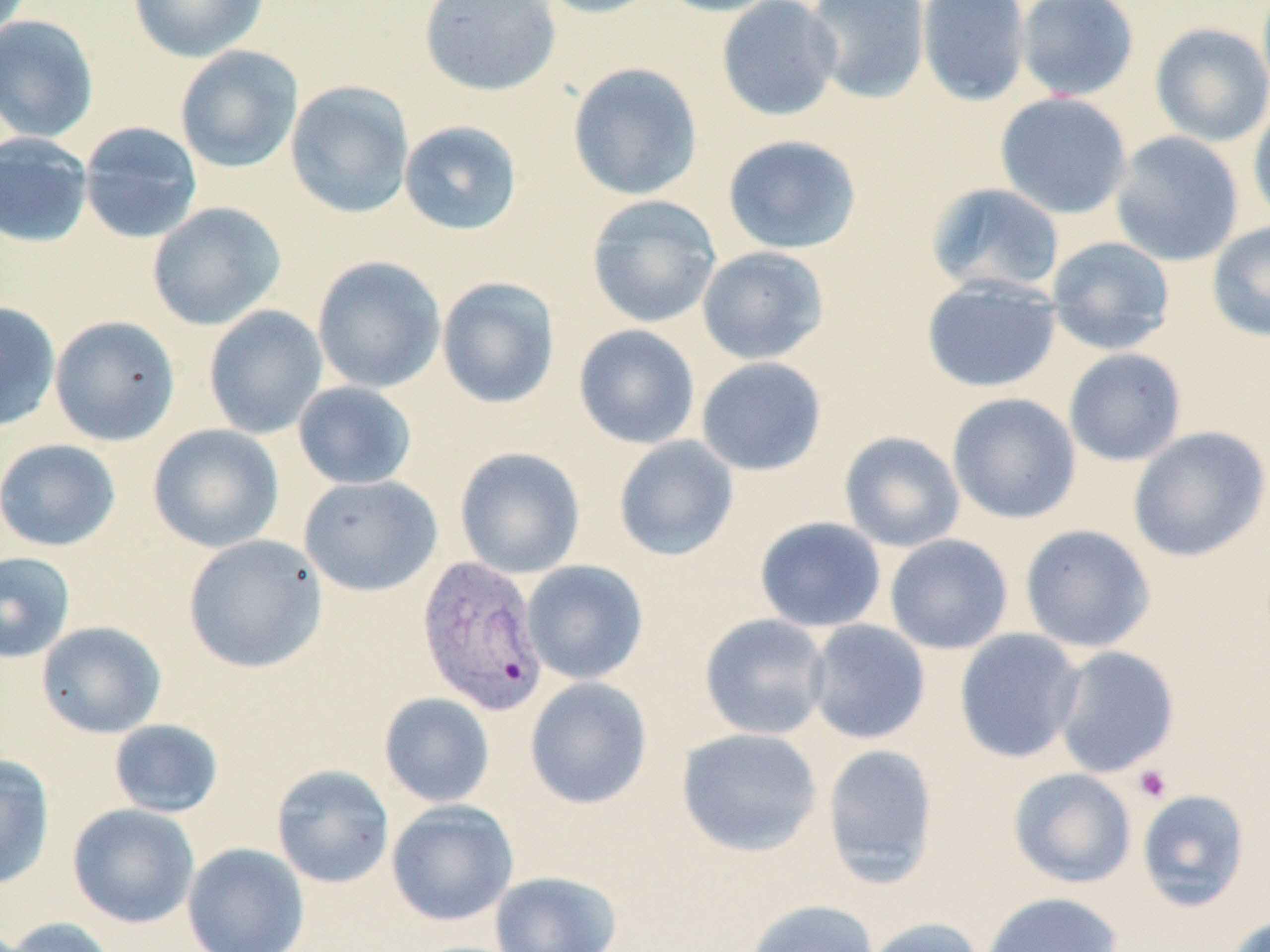

slide-level diagnosis = Plasmodium vivax
field of view = one of a larger specimen
magnification = 1000x
platelet locations = approximate bounding boxes as named x1/y1/x2/y2 corners in pixels: (x1=1133, y1=765, x2=1172, y2=803)
preparation = thin blood smear
image size = 1270×952 pixels
stain = May-Grünwald-Giemsa
uninfected red blood cell locations = approximate bounding boxes as named x1/y1/x2/y2 corners in pixels: (x1=127, y1=0, x2=269, y2=62), (x1=419, y1=0, x2=561, y2=96), (x1=536, y1=0, x2=665, y2=19), (x1=654, y1=0, x2=785, y2=17), (x1=716, y1=0, x2=842, y2=121), (x1=804, y1=0, x2=931, y2=105), (x1=915, y1=0, x2=1032, y2=107), (x1=1015, y1=0, x2=1140, y2=102), (x1=0, y1=14, x2=100, y2=143), (x1=1150, y1=22, x2=1270, y2=146), (x1=175, y1=45, x2=303, y2=173), (x1=567, y1=62, x2=703, y2=201), (x1=285, y1=81, x2=415, y2=218), (x1=994, y1=92, x2=1132, y2=219), (x1=1248, y1=100, x2=1270, y2=228), (x1=78, y1=121, x2=203, y2=244), (x1=398, y1=121, x2=523, y2=236), (x1=1110, y1=130, x2=1244, y2=267), (x1=0, y1=132, x2=94, y2=248), (x1=722, y1=134, x2=862, y2=254), (x1=925, y1=182, x2=1066, y2=297), (x1=586, y1=195, x2=722, y2=328), (x1=147, y1=202, x2=286, y2=331), (x1=1207, y1=221, x2=1270, y2=342), (x1=1046, y1=236, x2=1175, y2=355), (x1=697, y1=246, x2=830, y2=365), (x1=312, y1=256, x2=446, y2=393), (x1=921, y1=275, x2=1062, y2=393), (x1=436, y1=276, x2=560, y2=409), (x1=0, y1=302, x2=61, y2=432), (x1=203, y1=305, x2=328, y2=440), (x1=50, y1=316, x2=180, y2=446), (x1=573, y1=324, x2=700, y2=449), (x1=1063, y1=348, x2=1187, y2=466), (x1=695, y1=357, x2=827, y2=476), (x1=292, y1=381, x2=417, y2=490), (x1=947, y1=393, x2=1081, y2=524), (x1=147, y1=424, x2=284, y2=552), (x1=1128, y1=425, x2=1270, y2=563), (x1=838, y1=431, x2=965, y2=553), (x1=613, y1=435, x2=739, y2=561), (x1=0, y1=438, x2=121, y2=552), (x1=454, y1=446, x2=586, y2=579), (x1=299, y1=474, x2=443, y2=596), (x1=754, y1=516, x2=886, y2=632), (x1=1019, y1=524, x2=1156, y2=653), (x1=183, y1=534, x2=327, y2=673), (x1=884, y1=534, x2=1013, y2=655), (x1=0, y1=551, x2=77, y2=664), (x1=521, y1=559, x2=648, y2=685), (x1=699, y1=613, x2=832, y2=740), (x1=805, y1=619, x2=931, y2=744), (x1=36, y1=621, x2=166, y2=739), (x1=954, y1=628, x2=1086, y2=763), (x1=1051, y1=645, x2=1179, y2=778), (x1=524, y1=677, x2=652, y2=809), (x1=378, y1=692, x2=495, y2=808), (x1=108, y1=719, x2=224, y2=818), (x1=676, y1=727, x2=822, y2=856), (x1=821, y1=742, x2=939, y2=886), (x1=0, y1=754, x2=55, y2=890), (x1=271, y1=764, x2=394, y2=888), (x1=1008, y1=768, x2=1136, y2=888), (x1=1136, y1=789, x2=1250, y2=912), (x1=386, y1=799, x2=518, y2=926), (x1=67, y1=803, x2=200, y2=928), (x1=182, y1=842, x2=310, y2=952), (x1=490, y1=870, x2=622, y2=952), (x1=981, y1=891, x2=1123, y2=952), (x1=745, y1=899, x2=878, y2=952), (x1=1222, y1=914, x2=1270, y2=952), (x1=2, y1=916, x2=121, y2=952), (x1=864, y1=917, x2=985, y2=952)
modality = optical microscopy
Plasmodium vivax-infected red blood cell locations = approximate bounding boxes as named x1/y1/x2/y2 corners in pixels: (x1=416, y1=554, x2=549, y2=715)